Classify this cell by malaria status.
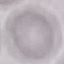

It is uninfected.

Summary:
  - Image type: cell patch, automatically extracted from a larger field of view and resized to 64 × 64 pixels
  - Capture: smartphone camera at the microscope eyepiece
  - Stain: Giemsa
  - Preparation: thin smear